Point out every Plasmodium parasite.
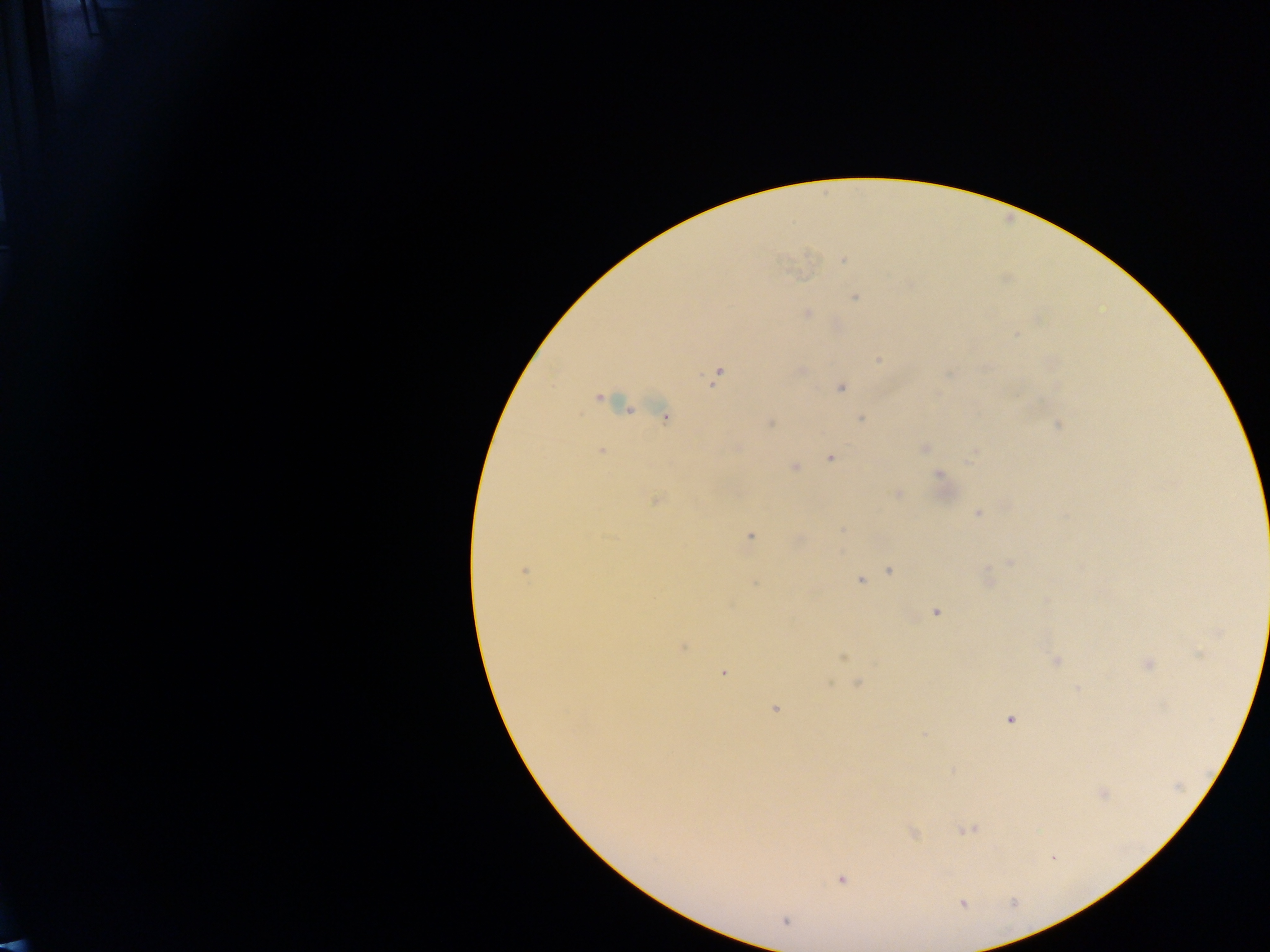
Approximate centers as (x, y) in pixels.
Plasmodium parasites: (843, 261), (855, 297), (806, 313), (1016, 335), (879, 359), (801, 371), (717, 374), (841, 389), (598, 398), (665, 417), (860, 419), (770, 422), (1059, 425), (924, 448), (602, 451), (830, 458), (795, 467), (940, 475), (897, 493), (655, 500), (978, 513), (750, 536), (1009, 563), (890, 571), (524, 572), (860, 580), (936, 612), (685, 647), (843, 658), (1056, 660), (1148, 664), (724, 672), (857, 684), (775, 709), (1011, 719), (1104, 793), (967, 830), (913, 834), (841, 881), (963, 904), (785, 921).

preparation: thick blood smear
capture: mobile-phone photograph through a microscope
country: Ghana
field_of_view: single
image_size: 1270×952 pixels